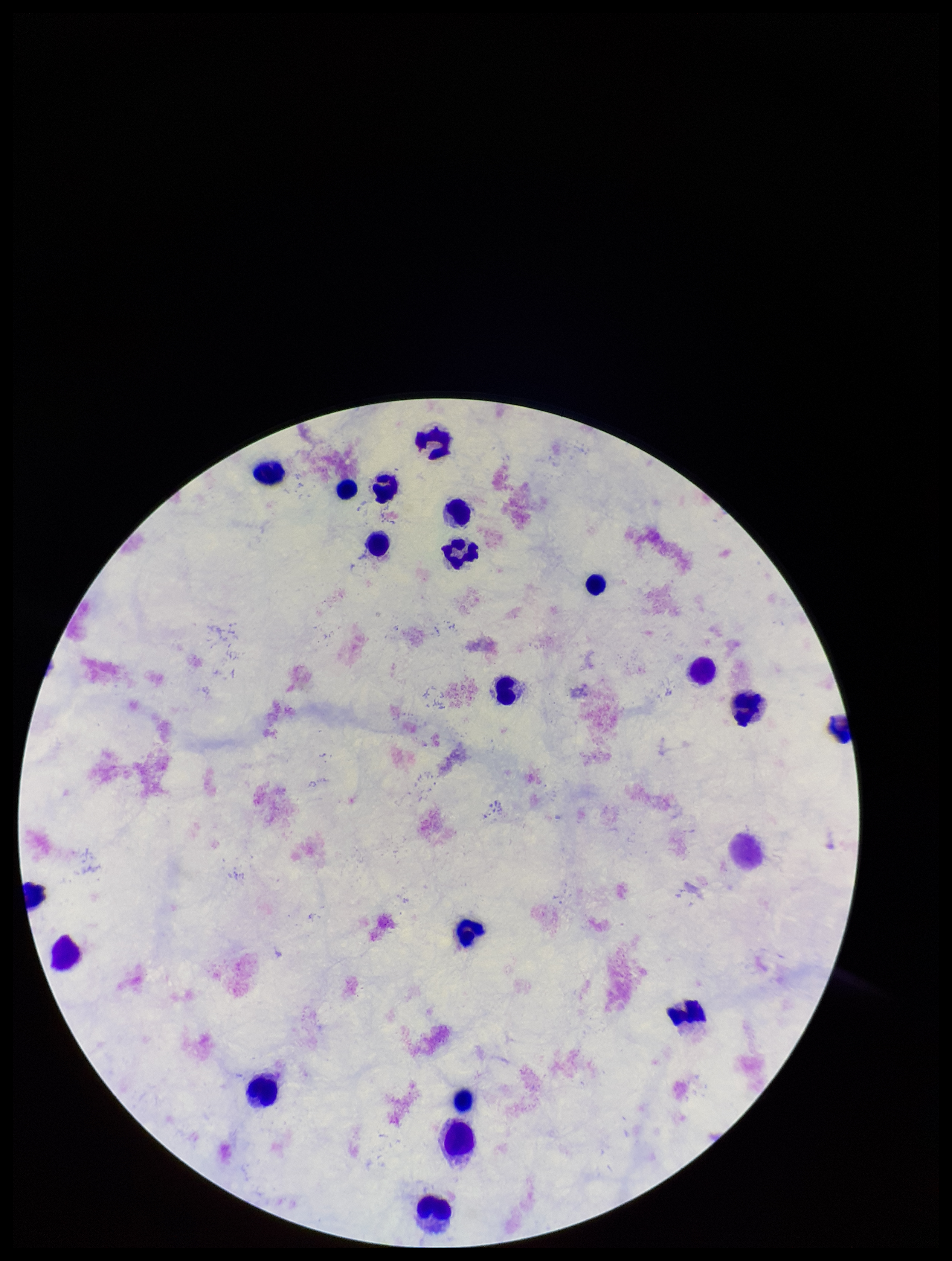
{
  "field_of_view": "single",
  "stain": "Giemsa",
  "preparation": "thick smear",
  "leukocyte_count": 20,
  "image_size": "952×1261 pixels",
  "capture": "smartphone photograph through the microscope eyepiece",
  "patient_malaria_status": "negative",
  "plasmodium_parasites": "none detected",
  "parasite_count": 0
}